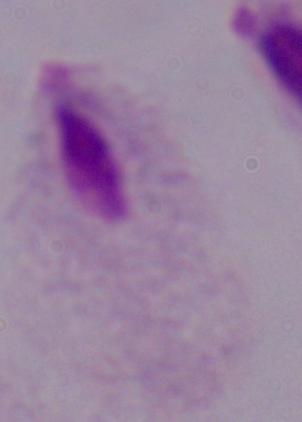

{
  "modality": "micrograph",
  "magnification": "1000x",
  "identification": "trichomonad"
}